Name the parasite shown.
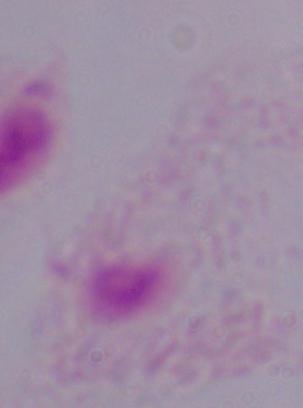

A trichomonad.

Captured at 1000x magnification. Micrograph.